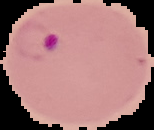
Summary:
  - Preparation: thin blood film
  - Image size: 154×130 pixels
  - Image type: cell region segmented out of the field of view; surrounding area masked to black
  - Result: malaria parasites detected